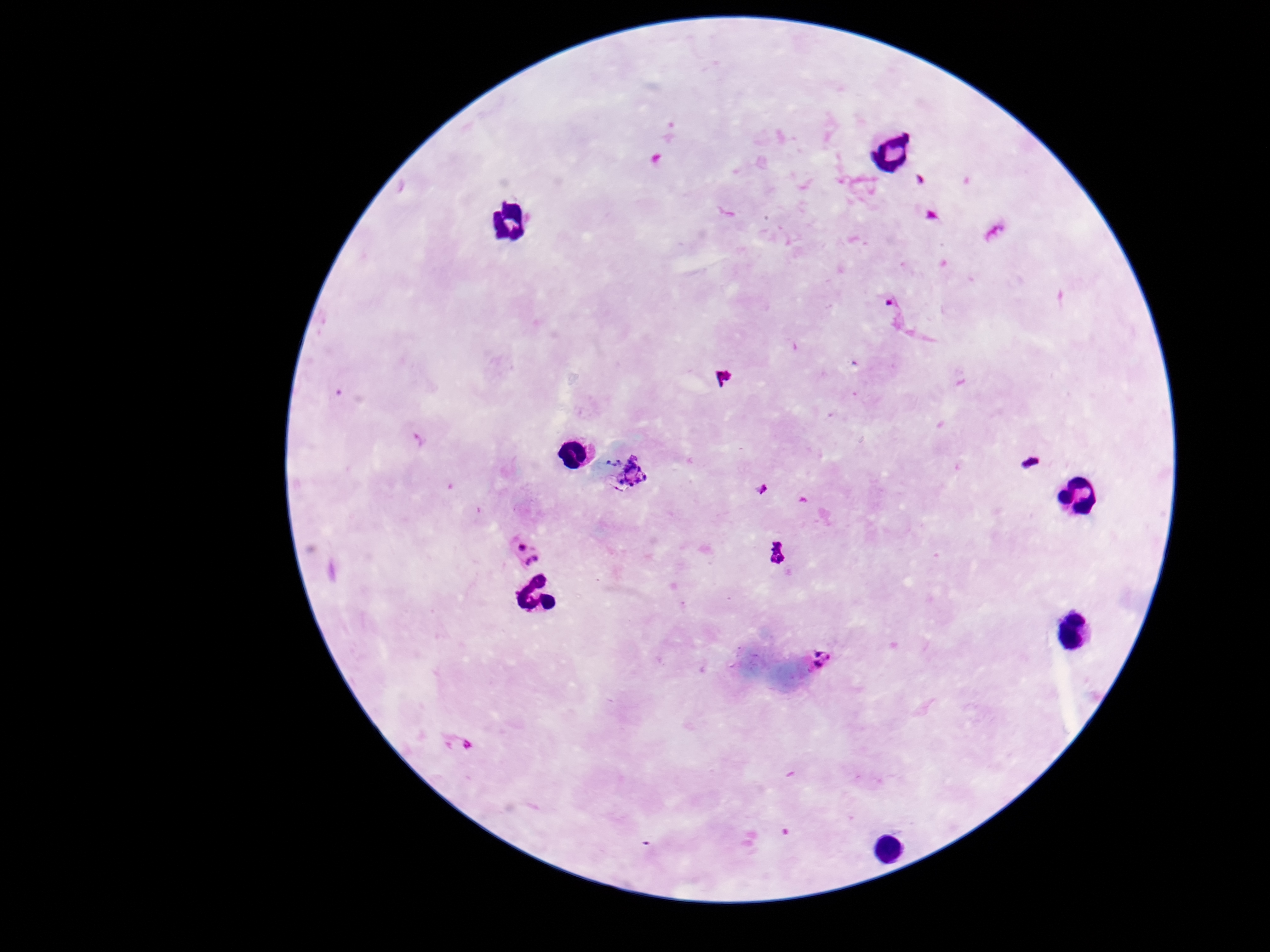

image size = 1270×952 pixels
capture = smartphone camera through the microscope eyepiece
stain = Giemsa
field of view = single
preparation = thick blood film
patient malaria status = positive
Plasmodium parasite locations = approximate centers as [x, y] in pixels: [627, 473], [526, 552], [815, 661], [457, 742]
magnification = 100x